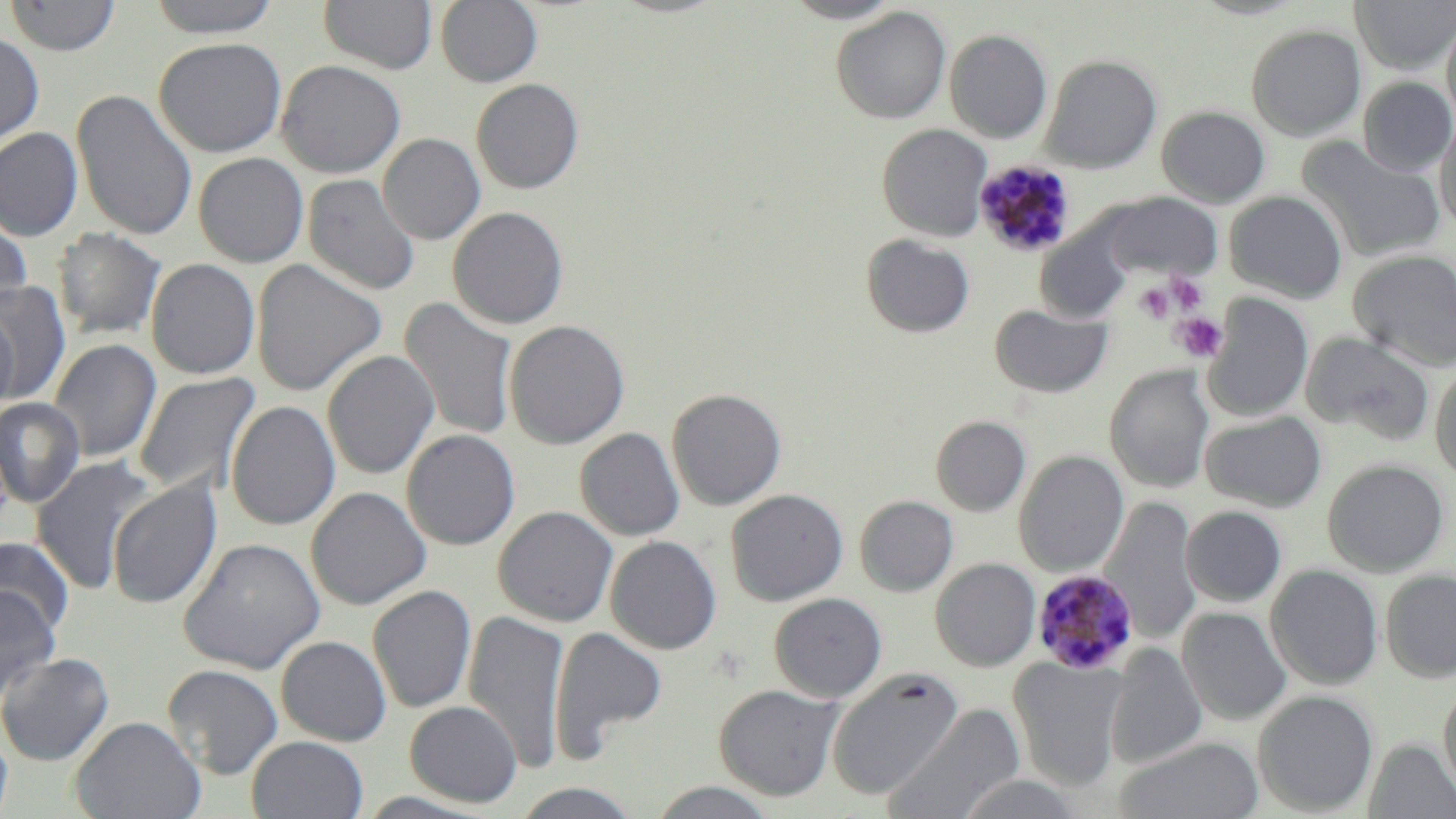
slide-level diagnosis = Plasmodium malariae
modality = optical microscopy
preparation = thin blood film
uninfected red blood cell locations = approximate bounding boxes as (x1,y1)-(x2,y2) corner pairs in pixels: (3,0)-(121,56), (146,0)-(282,37), (435,0)-(543,87), (780,0)-(904,24), (1351,0)-(1456,73), (319,1)-(437,74), (830,6)-(951,124), (1442,15)-(1456,129), (1246,23)-(1366,140), (944,29)-(1053,143), (0,31)-(44,147), (153,37)-(287,157), (945,40)-(1158,159), (1040,54)-(1162,173), (277,60)-(406,178), (1359,76)-(1456,176), (471,78)-(584,194), (71,89)-(197,241), (1157,106)-(1270,208), (1435,116)-(1456,235), (877,123)-(992,241), (0,127)-(83,241), (377,133)-(485,244), (1297,137)-(1446,262), (193,152)-(309,267), (303,173)-(420,296), (1225,191)-(1348,303), (1100,192)-(1221,280), (447,206)-(568,328), (0,213)-(32,319), (1035,225)-(1133,324), (54,227)-(165,339), (860,233)-(976,338), (1348,250)-(1456,371), (146,258)-(260,379), (250,259)-(386,397), (1,281)-(71,403), (1202,294)-(1313,422), (399,298)-(519,441), (989,304)-(1112,398), (0,309)-(19,416), (503,319)-(630,449), (1301,331)-(1436,446), (48,339)-(161,462), (322,350)-(439,479), (1430,364)-(1456,484), (1105,366)-(1214,493), (133,372)-(260,497), (666,387)-(787,510), (0,398)-(85,508), (226,400)-(340,530), (1201,409)-(1327,512), (931,415)-(1031,515), (575,427)-(685,541), (402,429)-(520,551), (1014,450)-(1128,577), (31,455)-(158,595), (1323,458)-(1449,576), (107,478)-(222,609), (305,486)-(430,610), (726,488)-(849,605), (855,495)-(958,595), (1101,497)-(1202,647), (1181,505)-(1286,607), (493,506)-(618,627), (605,535)-(722,654), (0,536)-(74,641), (178,536)-(325,674), (931,558)-(1041,671), (1266,565)-(1383,689), (1380,569)-(1456,682), (368,584)-(476,713), (0,585)-(61,703), (769,592)-(887,702), (1177,607)-(1292,725), (463,609)-(569,773), (550,626)-(667,760), (275,635)-(391,746), (1106,642)-(1207,769), (0,652)-(115,766), (1009,656)-(1127,790), (163,664)-(284,779), (826,667)-(964,800), (1439,679)-(1456,802), (714,683)-(843,800), (1253,690)-(1378,814), (404,700)-(522,807), (884,704)-(1024,819), (71,715)-(205,819), (0,725)-(13,819), (247,735)-(368,818), (1114,736)-(1264,819), (1365,739)-(1456,818), (646,781)-(780,818), (510,782)-(644,818)
magnification = 1000x
platelet locations = approximate bounding boxes as (x1,y1)-(x2,y2) corner pairs in pixels: (1165,273)-(1209,313), (1135,282)-(1175,322), (1171,311)-(1228,362)
stain = May-Grünwald-Giemsa
image size = 1456×819 pixels
field of view = single
Plasmodium malariae-infected red blood cell locations = approximate bounding boxes as (x1,y1)-(x2,y2) corner pairs in pixels: (974,160)-(1076,258), (1032,568)-(1139,674)